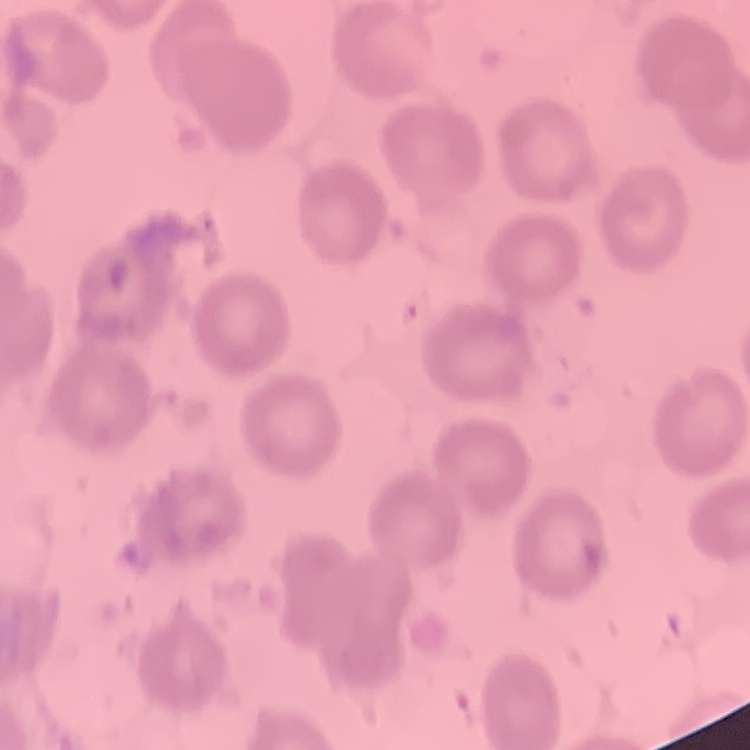
Summary:
  - Red blood cell morphology: no rouleaux formation
  - Preparation: thin blood smear
  - Image type: one tile cut from a larger photomicrograph
  - Stain: Field's or Giemsa